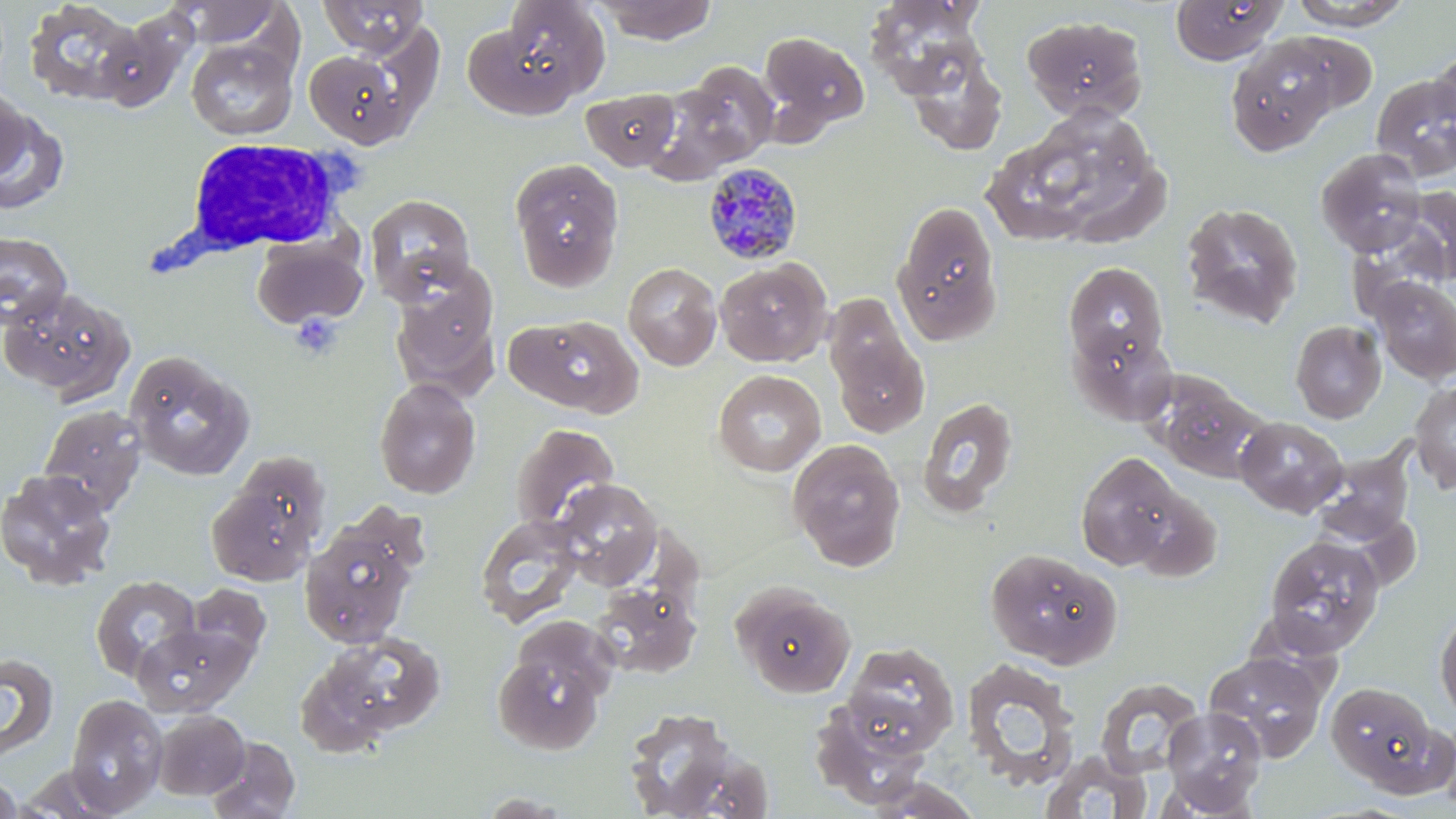
Approximate bounding boxes as (x1,y1)-(x2,y2) corner pairs in pixels. Uninfected red blood cell locations: (318,0)-(429,56), (596,0)-(717,44), (1290,0)-(1409,29), (22,1)-(144,106), (173,1)-(282,48), (864,1)-(987,97), (1171,1)-(1287,65), (469,2)-(609,114), (1022,15)-(1149,122), (95,17)-(192,114), (758,30)-(870,139), (1279,30)-(1381,119), (1225,37)-(1340,156), (186,39)-(297,140), (904,45)-(1007,155), (304,49)-(409,148), (1430,50)-(1456,143), (663,62)-(780,175), (1371,74)-(1456,181), (0,85)-(28,180), (582,88)-(680,170), (0,105)-(69,216), (990,106)-(1166,253), (1316,148)-(1428,256), (510,158)-(624,291), (1401,186)-(1456,285), (365,194)-(475,304), (891,199)-(1004,346), (1180,202)-(1304,328), (0,232)-(73,328), (252,237)-(368,329), (715,259)-(832,367), (623,262)-(722,371), (1063,262)-(1169,373), (388,266)-(500,399), (1372,278)-(1456,383), (0,286)-(134,403), (823,294)-(931,440), (510,314)-(644,418), (1291,320)-(1387,423), (1069,326)-(1177,425), (125,351)-(253,481), (713,370)-(826,476), (1150,375)-(1269,483), (374,377)-(481,499), (1410,380)-(1456,493), (918,396)-(1019,517), (38,404)-(148,514), (1235,416)-(1347,517), (511,423)-(619,535), (788,439)-(906,571), (1307,444)-(1418,548), (1074,452)-(1193,573), (0,469)-(118,590), (205,477)-(320,585), (554,478)-(663,588), (475,513)-(585,628), (299,518)-(420,649), (1267,533)-(1390,658), (985,548)-(1122,669), (90,575)-(202,683), (732,581)-(857,697), (185,583)-(271,667), (590,583)-(701,679), (1434,607)-(1456,720), (132,622)-(251,716), (310,631)-(447,742), (492,635)-(612,756), (842,641)-(959,754), (1203,650)-(1330,761), (0,652)-(59,759), (959,659)-(1081,788), (1094,678)-(1204,778), (1326,681)-(1443,791), (66,694)-(167,814), (808,699)-(932,808), (622,706)-(742,818), (1161,707)-(1267,814), (152,709)-(250,800), (206,736)-(301,819), (1040,750)-(1153,819), (12,766)-(130,817), (0,770)-(21,819), (861,775)-(985,817). Plasmodium malariae-infected red blood cell locations: (707,162)-(809,266). White blood cell locations: (169,135)-(359,267). Slide-level diagnosis: Plasmodium malariae. One field of a larger specimen. Image is 1456×819 pixels. Thin blood smear. 1000x magnification. May-Grünwald-Giemsa stain. Optical microscopy.